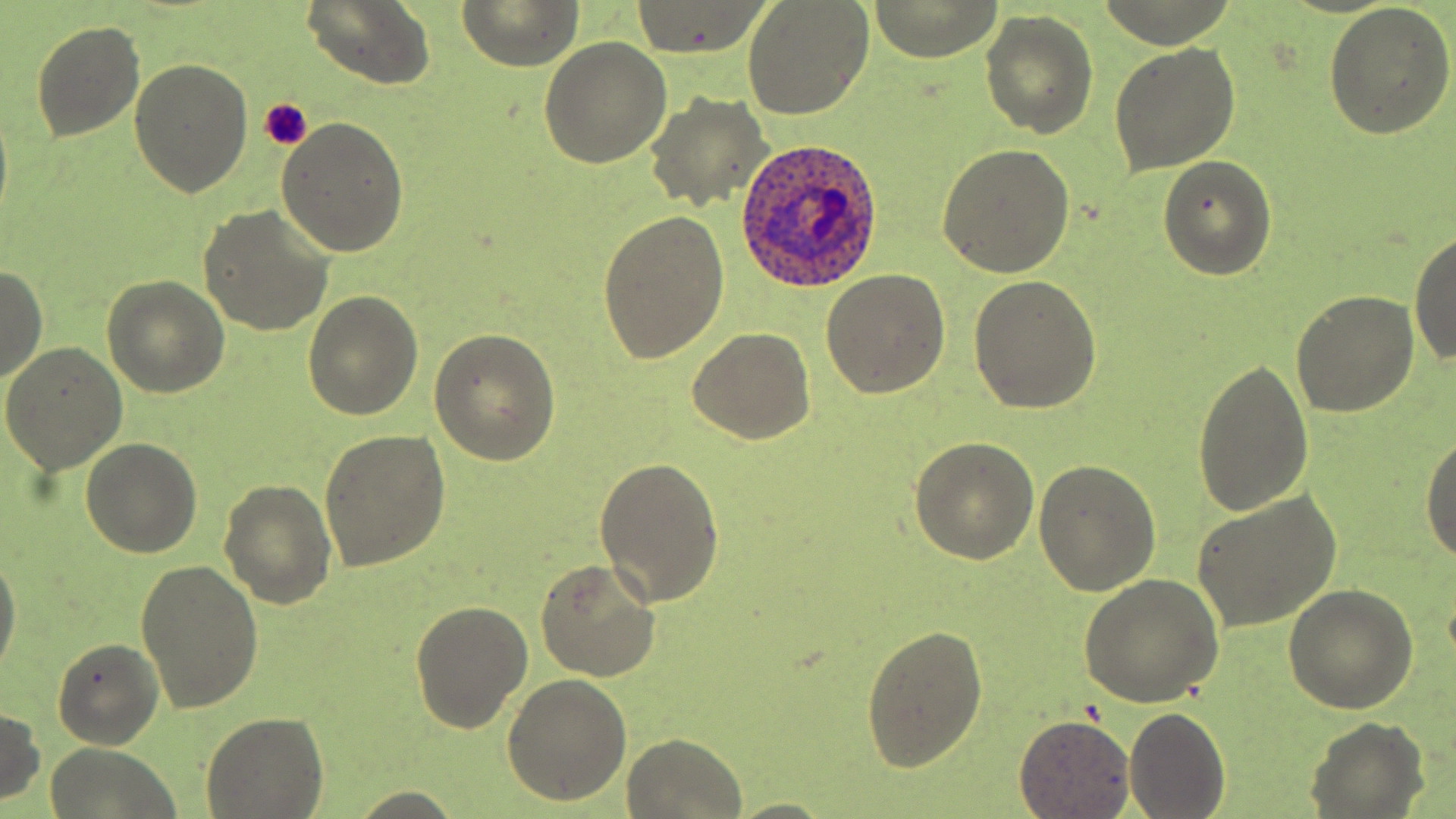
Summary:
  - Coordinate format: approximate bounding boxes as (x1, y1, x2, y2) in pixels
  - Plasmodium ovale-infected red blood cell locations: (735, 137, 884, 291)
  - Platelet locations: (257, 98, 311, 149)
  - Uninfected red blood cell locations: (742, 0, 876, 120), (867, 0, 1004, 62), (301, 1, 435, 90), (459, 1, 582, 69), (630, 2, 773, 60), (1323, 3, 1456, 139), (980, 10, 1098, 138), (30, 19, 146, 142), (539, 38, 673, 170), (1109, 45, 1241, 175), (129, 58, 253, 198), (645, 91, 772, 213), (277, 116, 409, 258), (937, 144, 1076, 278), (1157, 155, 1276, 279), (198, 205, 336, 337), (599, 211, 730, 363), (1409, 227, 1456, 369), (0, 266, 47, 385), (821, 267, 951, 398), (969, 274, 1101, 414), (102, 275, 230, 397), (1291, 289, 1420, 417), (304, 291, 424, 420), (431, 327, 562, 465), (687, 329, 817, 444), (1, 341, 129, 474), (1192, 359, 1315, 518), (1419, 425, 1456, 568), (318, 429, 450, 572), (80, 436, 202, 557), (909, 439, 1040, 565), (596, 455, 724, 608), (1035, 459, 1160, 598), (219, 479, 337, 609), (1190, 490, 1342, 633), (0, 549, 21, 680), (136, 559, 263, 713), (537, 559, 661, 682), (1080, 573, 1225, 707), (1284, 585, 1417, 714), (410, 599, 534, 735), (862, 622, 988, 772), (51, 637, 164, 750), (502, 674, 632, 805), (1122, 704, 1230, 818), (0, 706, 45, 806), (202, 710, 328, 817), (1014, 715, 1136, 817), (1306, 717, 1428, 817), (621, 733, 749, 819), (44, 743, 183, 818), (343, 789, 467, 819), (724, 797, 839, 818)
  - Slide-level diagnosis: Plasmodium ovale
  - Modality: optical microscopy
  - Stain: May-Grünwald-Giemsa
  - Preparation: thin blood smear
  - Image size: 1456×819 pixels
  - Field of view: one of a larger specimen
  - Magnification: 1000x